Locate every blood parasite and identify its species.
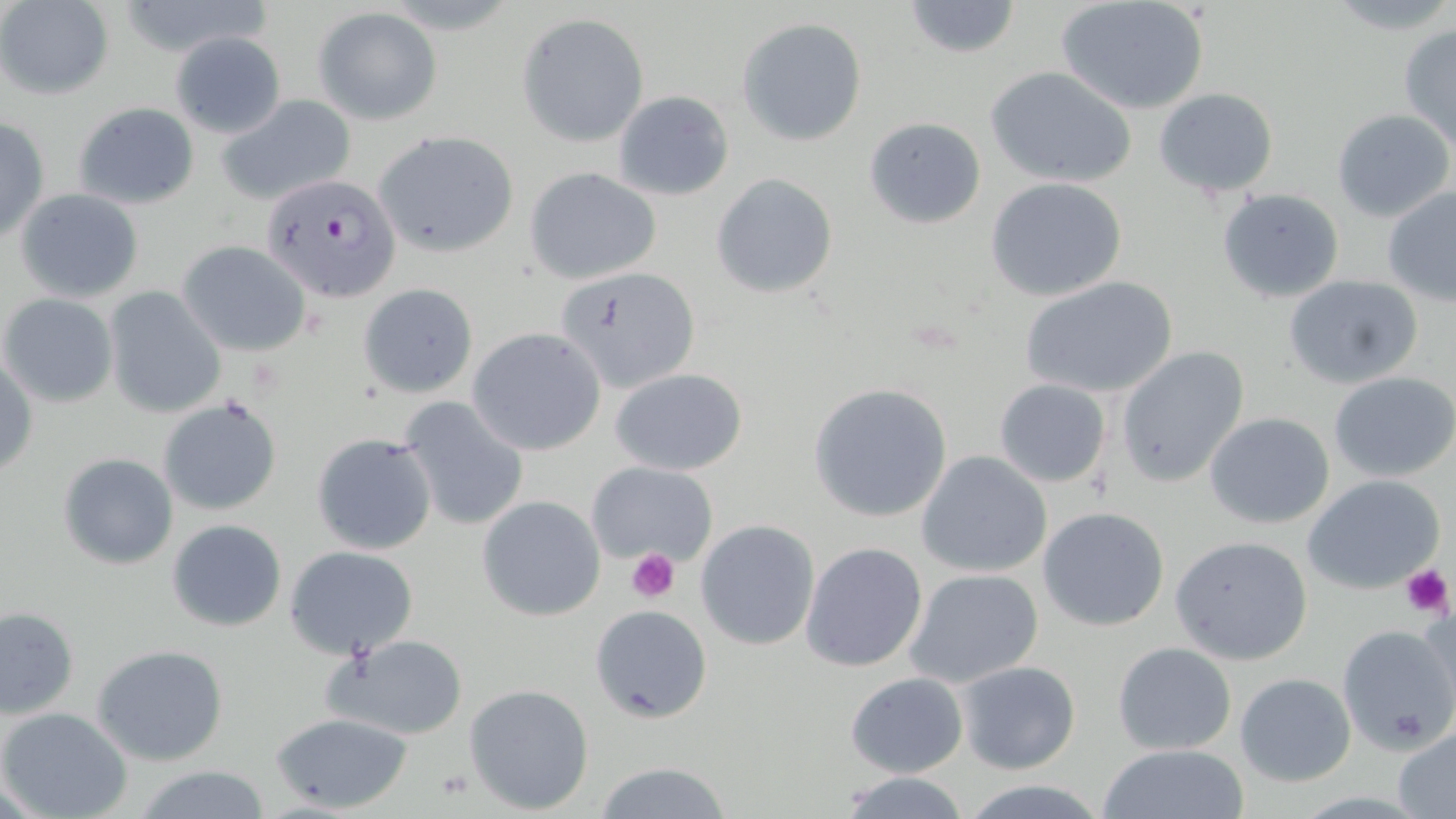
Approximate bounding boxes as (x1,y1)-(x2,y2) corner pairs in pixels.
Plasmodium falciparum-infected red blood cells: (264,172)-(401,302).
No Plasmodium ovale, Plasmodium malariae, Plasmodium vivax, Babesia divergens, or Trypanosoma brucei observed.

Uninfected red blood cell locations: (900,0)-(1024,58), (0,1)-(114,98), (1054,1)-(1209,115), (315,8)-(441,125), (518,13)-(648,145), (738,17)-(867,145), (1398,24)-(1456,152), (169,32)-(286,138), (986,66)-(1137,189), (1155,87)-(1278,197), (613,90)-(735,202), (214,93)-(358,204), (71,101)-(200,209), (1332,107)-(1454,222), (0,117)-(49,243), (865,117)-(987,229), (372,129)-(520,258), (524,166)-(662,284), (712,173)-(838,299), (986,178)-(1130,302), (1382,185)-(1456,306), (14,188)-(145,304), (1216,188)-(1346,302), (177,240)-(312,356), (555,266)-(702,394), (1283,273)-(1425,389), (1022,275)-(1179,400), (359,283)-(478,396), (104,289)-(226,419), (1,293)-(119,407), (467,328)-(606,456), (1115,345)-(1250,488), (0,357)-(38,480), (609,367)-(749,476), (1329,371)-(1456,480), (994,378)-(1110,489), (809,382)-(952,524), (158,394)-(283,516), (397,396)-(530,532), (1204,412)-(1334,528), (311,432)-(436,556), (917,449)-(1052,577), (58,452)-(178,570), (586,459)-(719,567), (1304,473)-(1444,594), (477,495)-(605,621), (1037,507)-(1170,630), (167,519)-(287,632), (695,521)-(820,650), (1170,534)-(1316,666), (800,542)-(928,671), (285,546)-(418,659), (904,568)-(1045,689), (589,605)-(714,724), (1,607)-(79,719), (1336,623)-(1456,755), (322,634)-(469,742), (1112,641)-(1238,753), (92,643)-(229,765), (955,660)-(1081,775), (844,671)-(968,777), (1235,673)-(1357,787), (465,682)-(596,814), (0,707)-(132,819), (273,712)-(414,813), (1392,725)-(1456,819), (1097,743)-(1251,819), (592,761)-(735,818), (132,765)-(274,819), (834,771)-(972,819), (957,780)-(1115,817). Platelet locations: (626,549)-(680,603), (1398,561)-(1452,618). Slide-level diagnosis: Plasmodium falciparum. Single field of view. May-Grünwald-Giemsa stain. Image is 1456×819 pixels. Light microscopy. Thin blood smear. Captured at 1000x magnification.